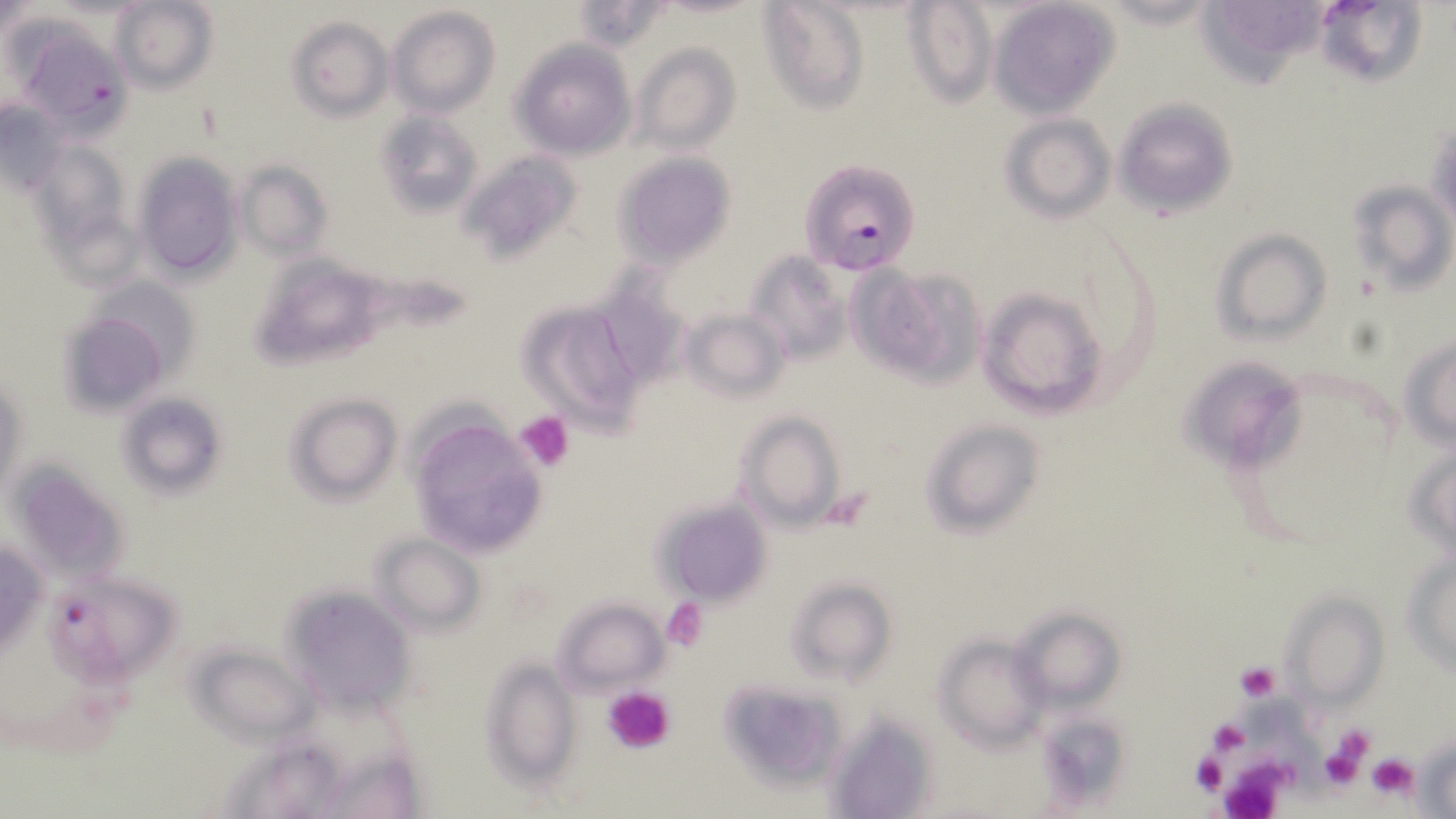
Approximate bounding boxes as (x1, y1, x2, y2) in pixels. Uninfected red blood cell locations: (109, 0, 218, 93), (759, 0, 869, 114), (902, 0, 998, 107), (987, 0, 1122, 116), (1195, 0, 1325, 84), (1313, 1, 1426, 87), (569, 2, 670, 51), (388, 7, 499, 118), (288, 16, 394, 121), (20, 31, 135, 143), (509, 40, 635, 159), (630, 41, 741, 157), (1112, 97, 1239, 222), (0, 100, 71, 199), (373, 110, 482, 218), (999, 115, 1116, 221), (1426, 120, 1455, 238), (29, 140, 132, 256), (460, 149, 581, 261), (617, 153, 735, 265), (132, 154, 242, 281), (235, 161, 332, 261), (1347, 176, 1453, 295), (1209, 228, 1333, 345), (245, 252, 393, 372), (744, 252, 850, 364), (850, 265, 981, 388), (591, 273, 692, 392), (82, 276, 203, 388), (975, 283, 1109, 421), (517, 299, 647, 430), (680, 306, 791, 404), (58, 311, 172, 416), (1401, 334, 1456, 450), (1181, 363, 1307, 471), (1, 375, 27, 501), (116, 392, 227, 499), (284, 392, 401, 503), (733, 409, 848, 533), (406, 414, 549, 558), (919, 418, 1045, 538), (1407, 439, 1456, 563), (7, 458, 132, 584), (652, 499, 772, 605), (1, 533, 46, 662), (371, 533, 486, 637), (1404, 546, 1456, 677), (54, 573, 185, 689), (786, 577, 896, 684), (284, 582, 415, 713), (1281, 590, 1389, 711), (550, 597, 667, 696), (1014, 605, 1124, 710), (934, 633, 1048, 748), (188, 641, 322, 748), (481, 657, 580, 787), (717, 680, 845, 789), (828, 710, 939, 818), (1033, 711, 1130, 810), (1414, 738, 1455, 816). Platelet locations: (516, 411, 574, 471), (823, 488, 874, 531), (660, 598, 709, 650), (1235, 661, 1280, 702), (602, 685, 677, 757), (1323, 721, 1377, 781), (1318, 740, 1368, 795), (1190, 749, 1227, 795), (1367, 754, 1416, 798), (1217, 758, 1294, 819). Plasmodium falciparum-infected red blood cell locations: (799, 159, 919, 273). Slide-level diagnosis: Plasmodium falciparum. Thin blood film. Image is 1456×819 pixels. Light microscopy. Single field of view. May-Grünwald-Giemsa-stained preparation. 1000x magnification.